Report the malaria status of this cell.
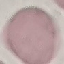
It is uninfected.

Photographed with a smartphone camera at the microscope eyepiece. Giemsa-stained preparation. Automatically extracted cell patch, resized to 64 × 64 pixels. Thin blood film.